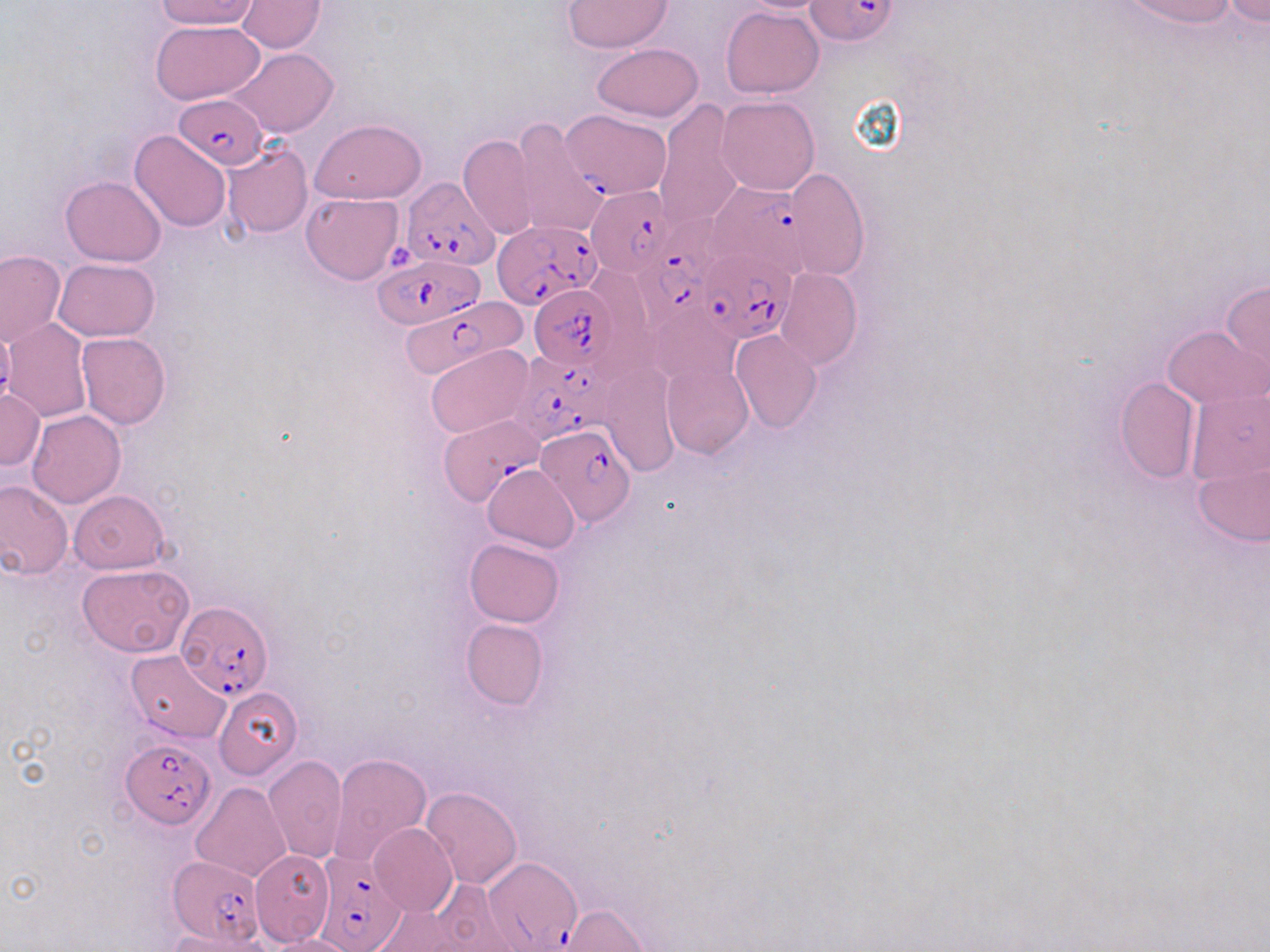
Approximate bounding boxes as [x1, y1, x2, y2] in pixels. Plasmodium falciparum-infected red blood cell locations (subset): [806, 0, 898, 46], [173, 93, 267, 168], [563, 110, 669, 198], [401, 178, 500, 270], [709, 181, 811, 275], [585, 186, 673, 278], [636, 215, 727, 324], [493, 220, 603, 313], [696, 247, 800, 345], [374, 255, 479, 329], [529, 284, 616, 372], [397, 294, 527, 379], [513, 349, 613, 444], [438, 417, 546, 511], [535, 423, 637, 528], [177, 601, 275, 702], [120, 739, 215, 828], [313, 851, 407, 952], [480, 855, 583, 951], [168, 856, 265, 944]. Platelet locations: [389, 243, 418, 270]. Uninfected red blood cell locations (subset): [154, 0, 259, 30], [1116, 0, 1242, 28], [234, 1, 329, 52], [563, 1, 672, 53], [1218, 1, 1270, 27], [722, 7, 824, 98], [151, 20, 265, 105], [592, 44, 703, 122], [226, 48, 337, 138], [716, 96, 819, 195], [653, 103, 745, 231], [513, 117, 608, 239], [311, 118, 426, 204], [130, 130, 233, 231], [458, 134, 538, 240], [222, 144, 313, 238], [780, 170, 868, 277], [59, 175, 166, 267], [301, 193, 404, 285], [0, 250, 66, 346], [52, 258, 160, 340], [776, 269, 861, 370], [1220, 279, 1270, 387], [4, 318, 94, 420], [1163, 325, 1266, 407], [730, 329, 822, 432], [76, 332, 171, 428], [424, 345, 533, 440], [661, 360, 754, 459], [603, 366, 678, 476], [1114, 377, 1199, 483], [1185, 384, 1269, 499], [0, 388, 44, 471], [26, 409, 126, 508], [1192, 459, 1270, 548], [483, 464, 580, 553], [0, 479, 73, 580], [68, 489, 169, 574], [464, 537, 566, 627], [76, 564, 193, 656], [461, 618, 547, 710], [126, 650, 232, 742], [213, 686, 302, 781], [329, 751, 432, 867], [264, 754, 348, 864], [191, 782, 291, 882], [421, 786, 521, 890], [370, 823, 458, 917], [420, 880, 522, 951], [556, 903, 652, 951], [164, 928, 271, 952], [262, 935, 359, 952]. Slide-level diagnosis: Plasmodium falciparum. Light microscopy. Single field of view. Captured at 1000x magnification. Thin blood smear. Image is 1270×952 pixels. May-Grünwald-Giemsa-stained preparation.